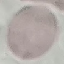

{
  "malaria_status": "uninfected",
  "image_type": "automatically extracted cell patch, resized to 64 × 64 pixels",
  "preparation": "thin smear",
  "stain": "Giemsa",
  "capture": "smartphone through the microscope eyepiece"
}